Locate every Plasmodium vivax-infected red blood cell.
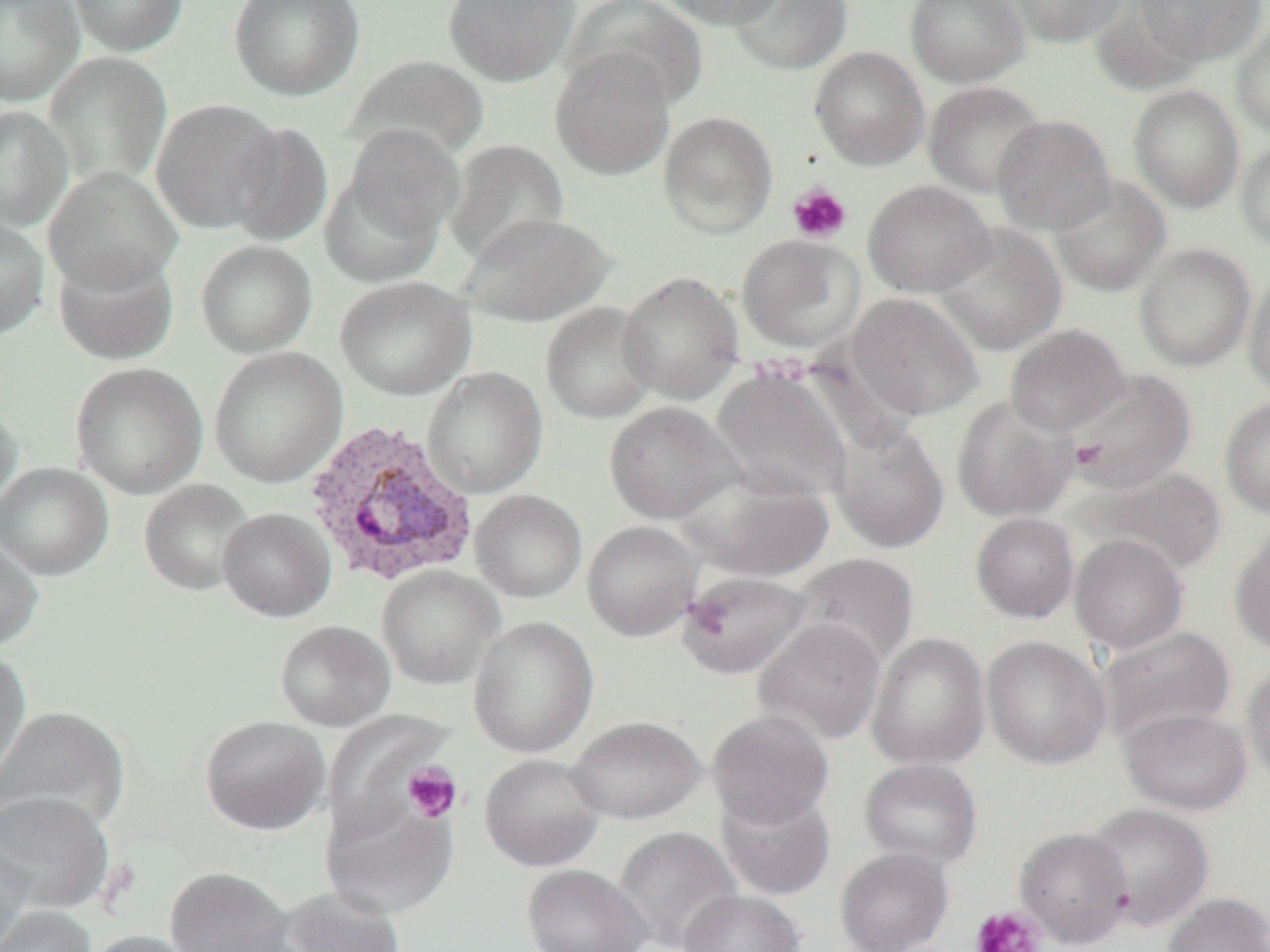
Approximate bounding boxes as (x1,y1)-(x2,y2) corner pairs in pixels.
Plasmodium vivax-infected red blood cells: (302,419)-(480,588).

Summary:
  - Uninfected red blood cell locations: (0,0)-(85,106), (69,0)-(188,57), (229,0)-(365,101), (443,0)-(580,86), (565,0)-(707,110), (656,0)-(788,29), (729,0)-(852,75), (905,0)-(1030,87), (1000,0)-(1129,47), (1134,0)-(1267,66), (1230,21)-(1270,139), (809,46)-(930,170), (550,47)-(676,180), (44,51)-(173,190), (346,55)-(490,163), (923,81)-(1048,198), (1127,84)-(1245,213), (150,98)-(282,233), (0,105)-(73,231), (658,110)-(778,238), (992,114)-(1117,236), (224,121)-(334,247), (342,124)-(465,247), (1234,138)-(1270,252), (445,139)-(569,267), (43,167)-(184,294), (319,168)-(445,287), (1049,176)-(1171,297), (863,180)-(996,298), (457,211)-(615,326), (0,215)-(50,339), (934,222)-(1067,356), (736,234)-(866,353), (195,239)-(318,358), (1134,243)-(1256,371), (53,247)-(179,365), (1243,269)-(1270,401), (617,270)-(745,404), (335,276)-(476,400), (846,293)-(983,421), (540,301)-(660,424), (1005,323)-(1130,436), (209,346)-(347,488), (70,362)-(208,499), (710,366)-(854,503), (422,367)-(548,499), (1067,369)-(1196,494), (951,395)-(1078,523), (1219,396)-(1270,518), (0,398)-(23,518), (603,401)-(742,524), (831,423)-(950,553), (0,462)-(114,580), (1081,467)-(1227,576), (679,472)-(835,581), (139,479)-(257,594), (470,489)-(588,603), (218,507)-(336,622), (970,512)-(1080,623), (582,520)-(703,641), (1230,524)-(1270,656), (1070,534)-(1188,653), (0,536)-(43,652), (790,553)-(919,670), (377,565)-(504,689), (675,570)-(815,680), (469,616)-(599,758), (752,619)-(887,746), (275,620)-(396,731), (1097,625)-(1236,743), (866,632)-(991,771), (981,635)-(1111,769), (0,645)-(32,788), (1241,661)-(1270,788), (0,705)-(131,834), (1119,707)-(1252,815), (707,710)-(835,829), (199,715)-(330,835), (567,715)-(707,825), (479,753)-(608,872), (858,758)-(984,870), (716,787)-(836,901), (0,791)-(115,915), (320,793)-(458,917), (1083,802)-(1215,931), (613,826)-(743,952), (1015,827)-(1134,948), (0,838)-(34,951), (835,847)-(953,952), (521,864)-(652,951), (164,866)-(294,952), (276,886)-(407,952), (679,889)-(805,952), (1161,892)-(1270,952), (0,906)-(96,952), (80,930)-(202,952)
  - Platelet locations: (787,182)-(852,244), (1070,439)-(1107,471), (686,596)-(732,640), (402,761)-(462,822), (970,905)-(1047,952)
  - Slide-level diagnosis: Plasmodium vivax
  - Field of view: single
  - Magnification: 1000x
  - Modality: light microscopy
  - Image size: 1270×952 pixels
  - Preparation: thin blood film